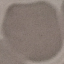

result = negative for malaria parasites
stain = Giemsa
preparation = thin blood film
image type = cell patch, automatically extracted from a larger field of view and resized to 64 × 64 pixels
capture = smartphone camera at the microscope eyepiece